Report the malaria status of this cell.
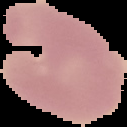
It is uninfected.

From a thin blood smear. Image is 127×127 pixels. Segmented cell region on a black background.